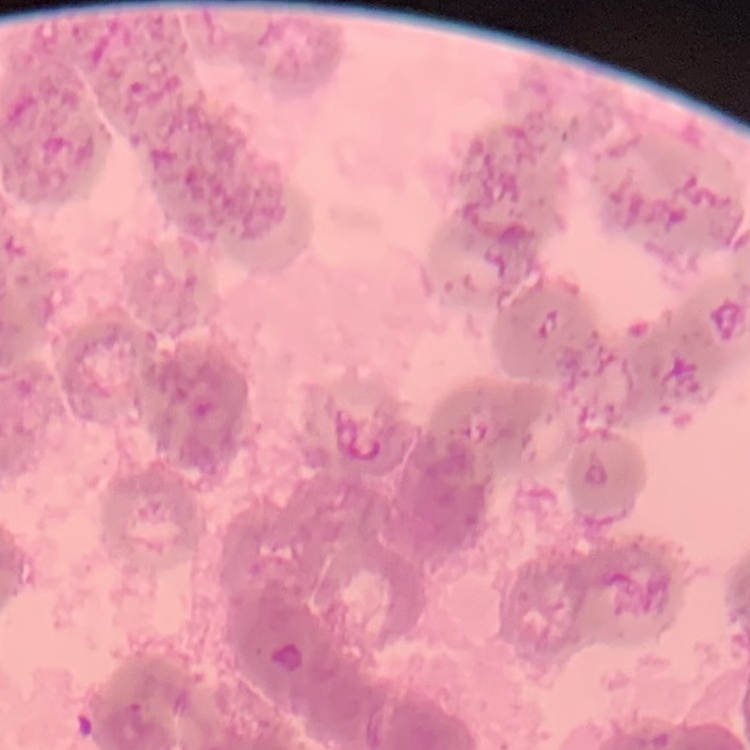

red blood cell morphology = rouleaux formation
stain = Field's or Giemsa
image type = one tile cut from a larger photomicrograph
preparation = thin peripheral smear